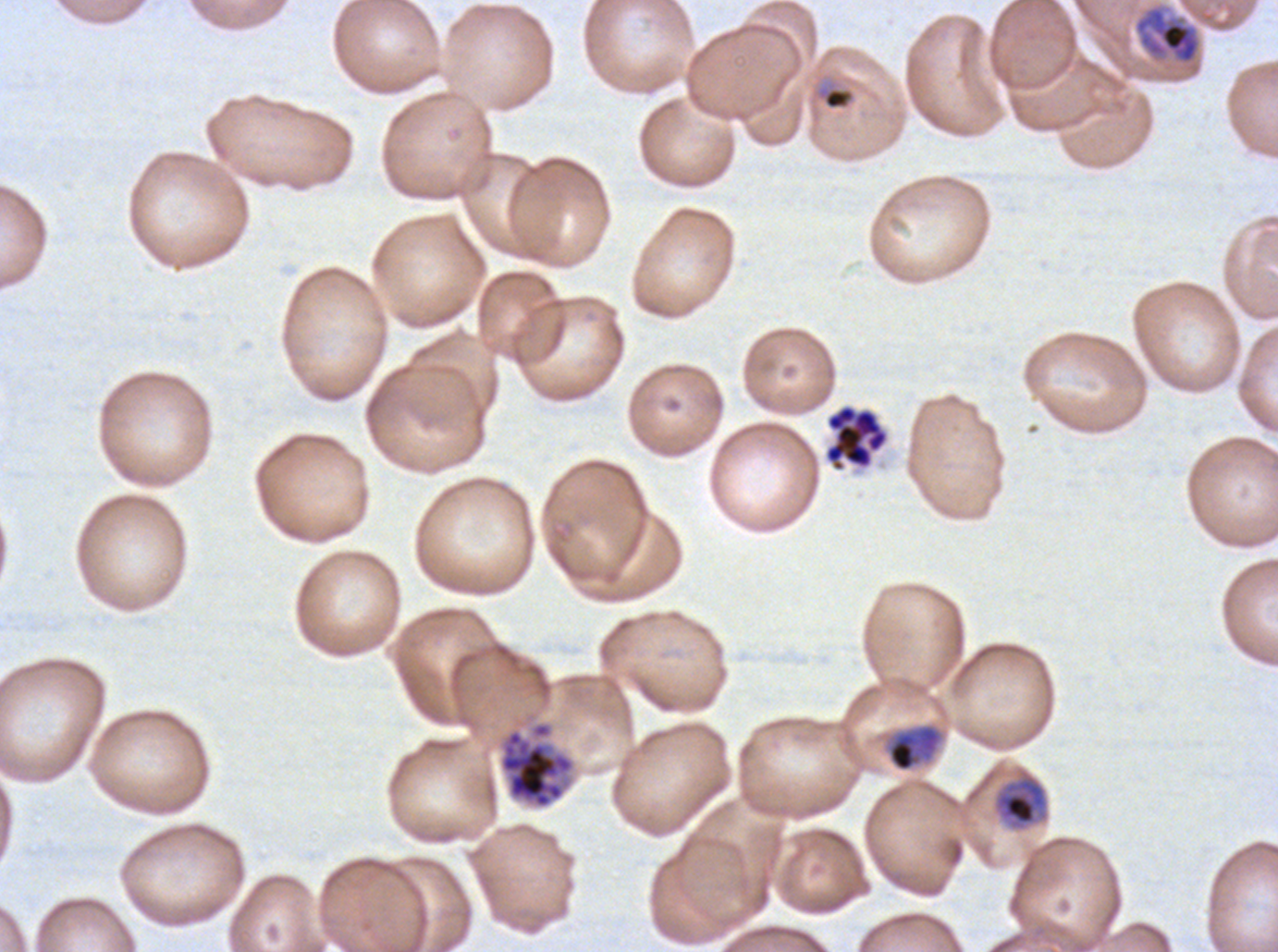

Approximate bounding rectangles given as corner coordinates in pixels from the top-left. Mid trophozoite locations: (x1=1134, y1=6, x2=1200, y2=65), (x1=887, y1=725, x2=941, y2=772), (x1=994, y1=775, x2=1048, y2=830). Late-ring/early-trophozoite locations: (x1=822, y1=87, x2=854, y2=111). Segmenter locations: (x1=824, y1=404, x2=889, y2=472). Late schizont locations: (x1=498, y1=720, x2=576, y2=810). Life-cycle stages observed: late-ring/early-trophozoite, mid trophozoite, late schizont, segmenter. Image is 1278×952 pixels. Plasmodium falciparum cultured ex vivo for 24 to 48 hours, from a patient in The Gambia. Giemsa stain. Thin blood film. A sub-image separated from a larger composite.